Classify this cell by malaria status.
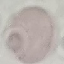

Uninfected.

stain = Giemsa
preparation = thin smear
image type = automatically extracted cell patch, resized to 64 × 64 pixels
capture = smartphone camera at the microscope eyepiece